Name the parasite shown.
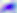
Toxoplasma gondii.

Photomicrograph. 400x magnification.